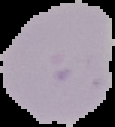

Summary:
  - Image size: 115×127 pixels
  - Preparation: thin blood film
  - Image type: cell region segmented out of the field of view; surrounding area masked to black
  - Malaria status: uninfected